Describe the morphology of the erythrocytes.
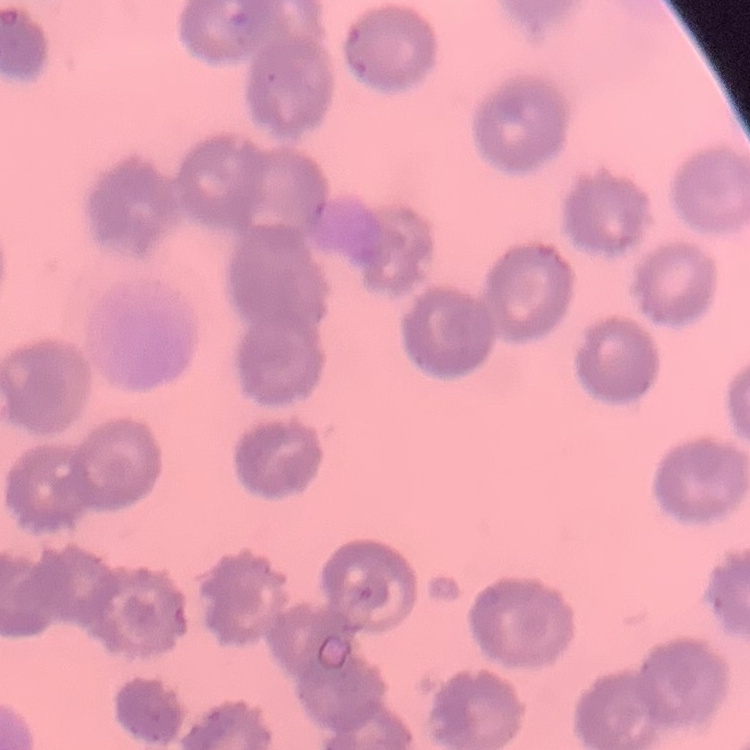
They show no rouleaux formation.

stain = Field's or Giemsa
preparation = thin peripheral smear
image type = square crop of a larger photomicrograph